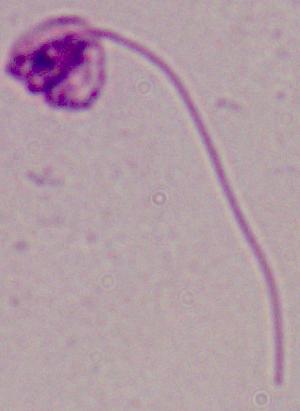 Captured at 1000x magnification. A Leishmania parasite is seen. Micrograph.